Give the position of every Plasmodium parasite.
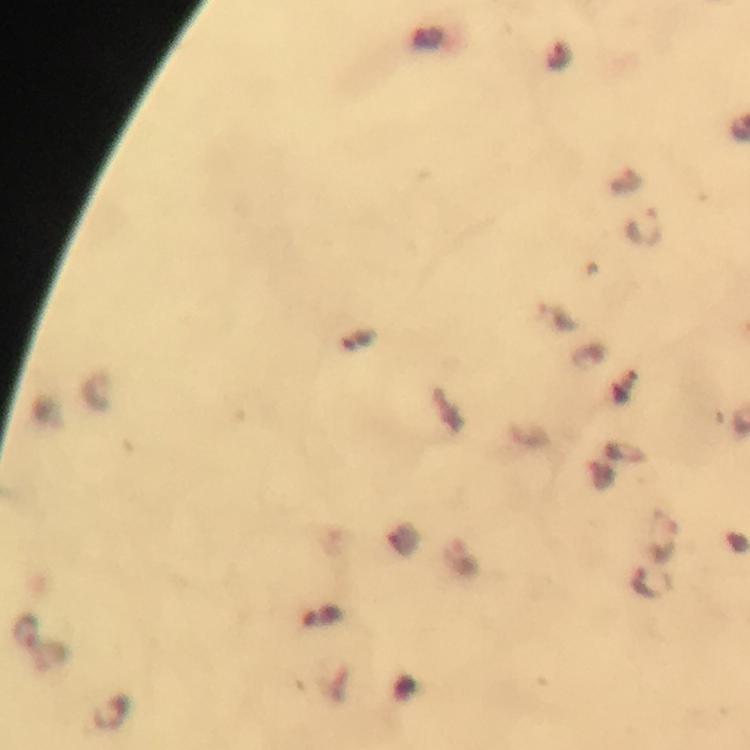
Approximate centers as {x, y} in pixels.
Plasmodium parasites: {559, 57}, {645, 229}, {648, 581}, {25, 632}.

{
  "immersion_oil": "used",
  "context": "from a diagnostic examination for malaria",
  "cropped_from": "a single field of view",
  "preparation": "thick blood smear",
  "magnification": "100x",
  "capture": "smartphone photograph through a microscope",
  "image_size": "750×750 pixels",
  "stain": "Giemsa"
}